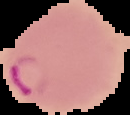
result = malaria parasites identified
image size = 130×115 pixels
preparation = thin blood film
image type = segmented cell region on a black background